Assess the morphology of the red blood cells.
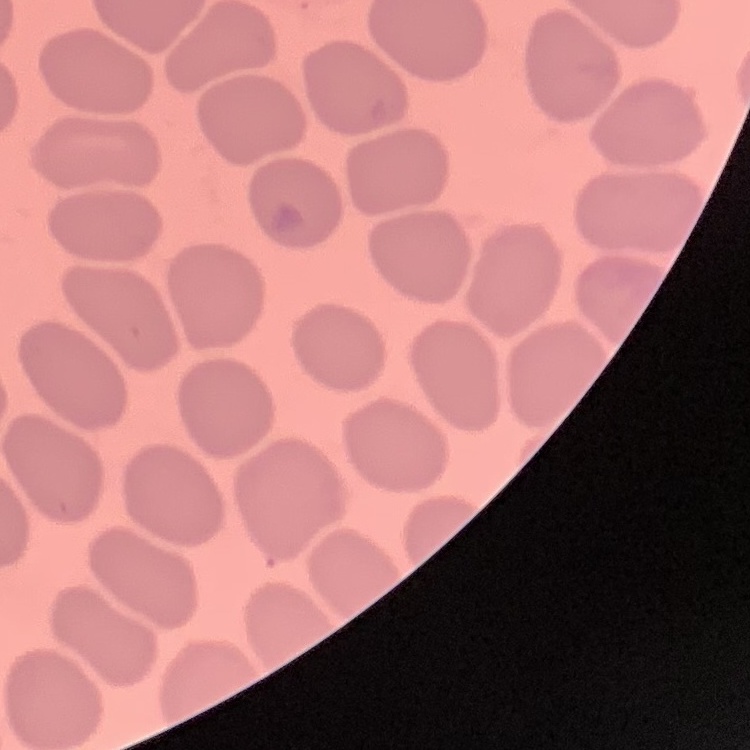

No rouleaux formation.

Summary:
  - Image type: square crop of a larger photomicrograph
  - Preparation: thin blood film
  - Stain: Field's or Giemsa